Assess this cell for malaria.
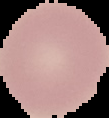
Uninfected.

image size = 109×118 pixels
image type = segmented cell region with the area outside set to black
preparation = thin blood film